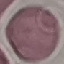
Summary:
  - Malaria status: uninfected
  - Stain: Giemsa
  - Capture: smartphone through the microscope eyepiece
  - Image type: automatically extracted cell patch, resized to 64 × 64 pixels
  - Preparation: thin smear